Assess the morphology of the red blood cells.
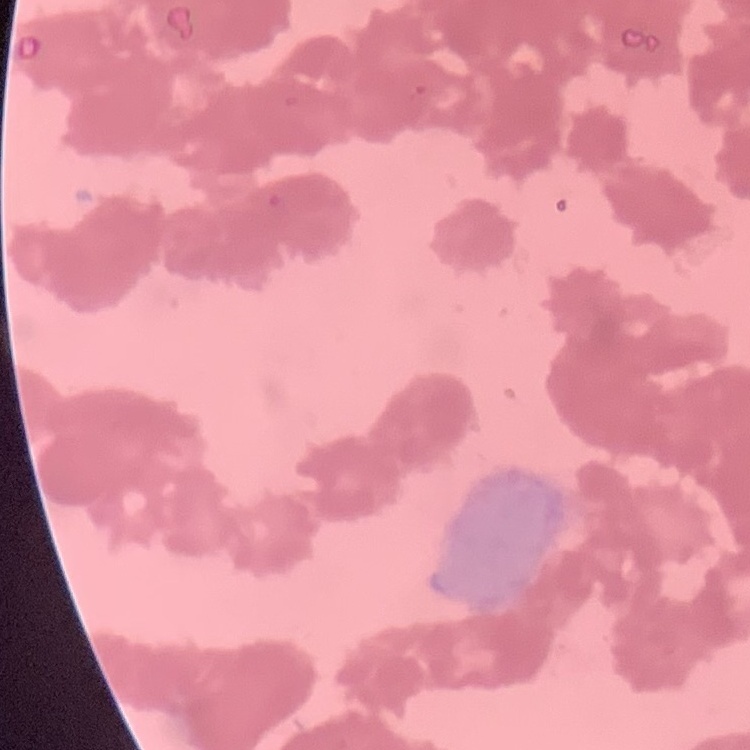
Rouleaux formation.

Stained with either Field's or Giemsa. Square crop of a larger photomicrograph. Thin peripheral smear.